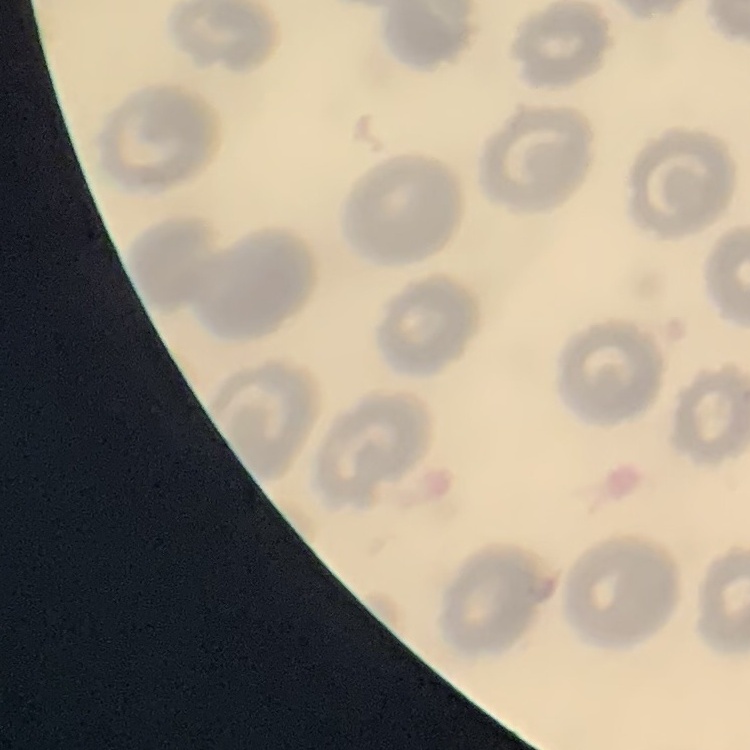
erythrocyte morphology = no rouleaux formation
preparation = thin blood smear
stain = Field's or Giemsa
image type = square crop of a larger photomicrograph